Report the malaria status.
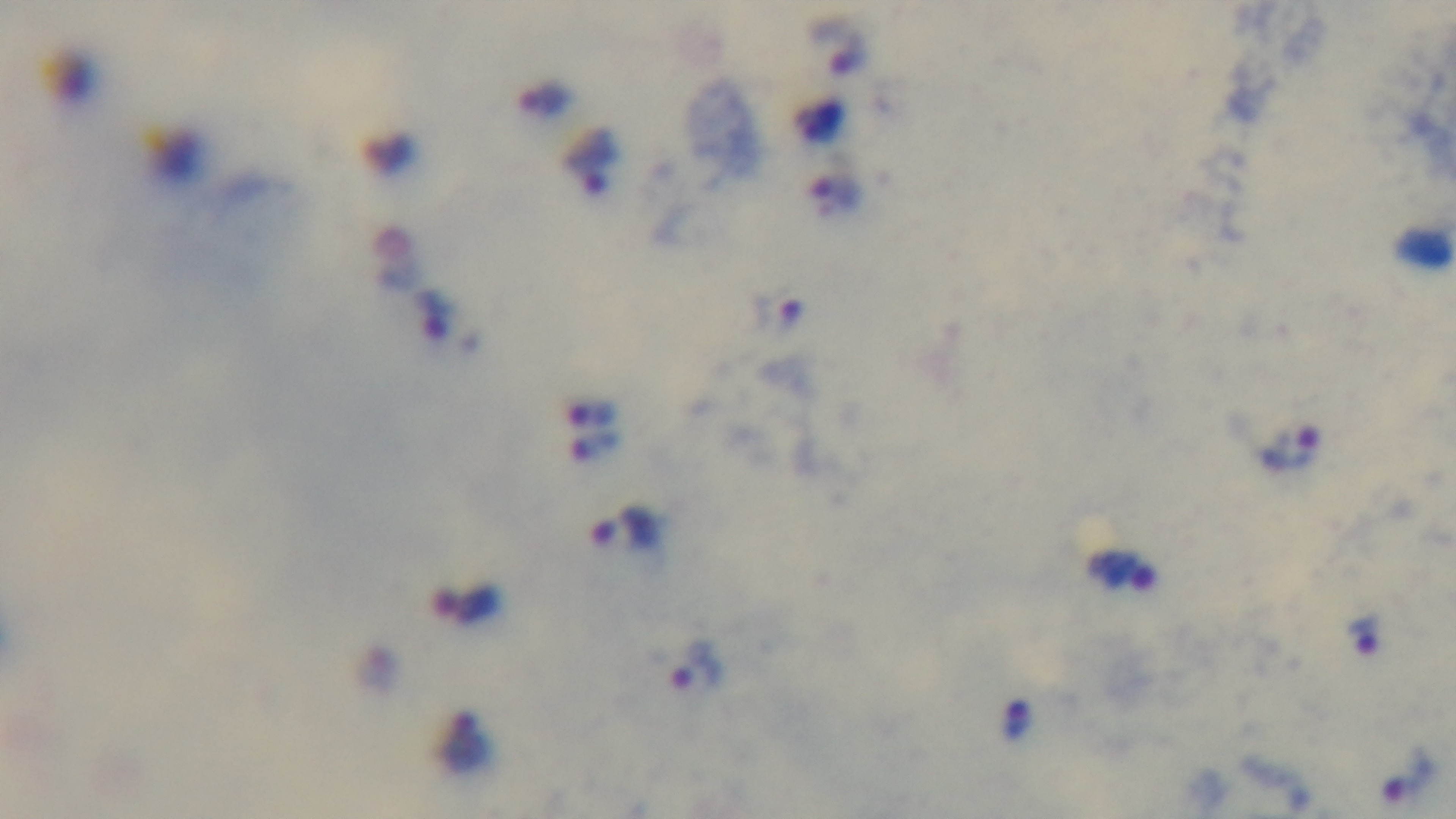

Infected.

Preparation: thick blood film. One field from the slide. Giemsa stain. Oil-immersion objective, 100x. Captured with a mounted 4K digital camera. Photomicrograph.